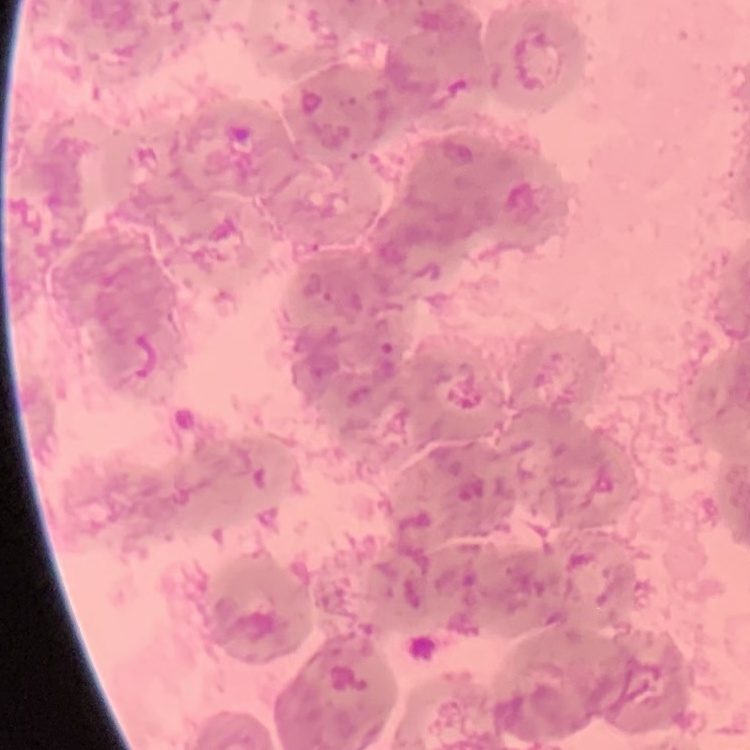

Summary:
  - Red blood cell morphology: rouleaux formation
  - Preparation: thin blood film
  - Image type: one tile cut from a larger photomicrograph
  - Stain: Field's or Giemsa